Name the cell type shown.
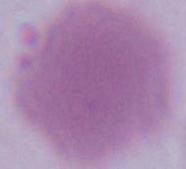
An erythrocyte.

Summary:
  - Magnification: 1000x
  - Modality: micrograph